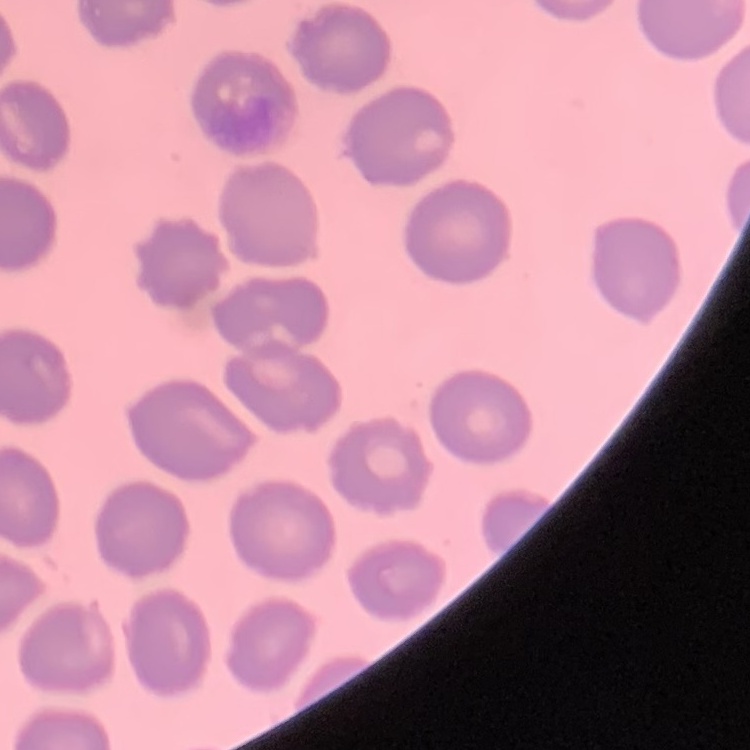

red blood cell morphology = no rouleaux formation
image type = square crop of a larger photomicrograph
preparation = thin blood smear
stain = Field's or Giemsa